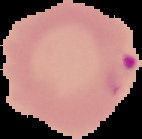
Malaria status: parasitized. The area outside the segmented cell region is set to black. Image is 142×139 pixels. From a thin blood film.